Identify the blood parasite species.
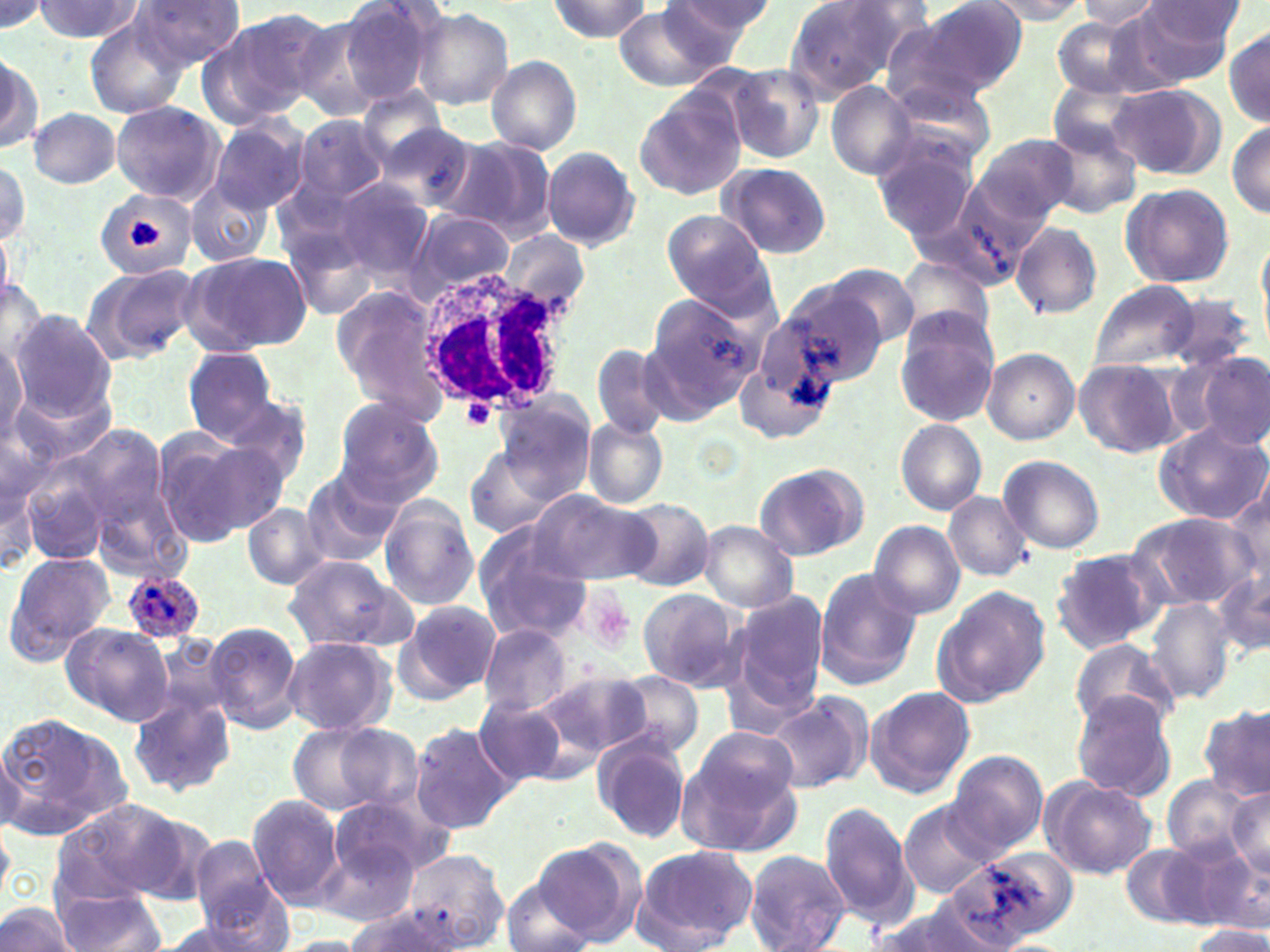
Plasmodium ovale.

Approximate bounding boxes as named x1/y1/x2/y2 corners in pixels. White blood cell locations: (x1=414, y1=260, x2=575, y2=418). Plasmodium ovale-infected red blood cell locations: (x1=122, y1=568, x2=205, y2=644). Platelet locations: (x1=130, y1=219, x2=160, y2=250), (x1=461, y1=399, x2=498, y2=433), (x1=582, y1=593, x2=634, y2=654). Uninfected red blood cell locations: (x1=337, y1=0, x2=446, y2=106), (x1=665, y1=0, x2=772, y2=55), (x1=782, y1=0, x2=915, y2=101), (x1=910, y1=0, x2=1028, y2=97), (x1=982, y1=0, x2=1092, y2=24), (x1=1076, y1=0, x2=1164, y2=30), (x1=35, y1=1, x2=142, y2=42), (x1=131, y1=1, x2=245, y2=71), (x1=547, y1=1, x2=652, y2=40), (x1=0, y1=2, x2=45, y2=31), (x1=612, y1=3, x2=737, y2=88), (x1=1131, y1=3, x2=1240, y2=83), (x1=411, y1=8, x2=513, y2=110), (x1=200, y1=11, x2=327, y2=123), (x1=83, y1=17, x2=190, y2=120), (x1=1051, y1=18, x2=1151, y2=98), (x1=880, y1=21, x2=1003, y2=120), (x1=1224, y1=26, x2=1269, y2=128), (x1=1, y1=54, x2=41, y2=154), (x1=486, y1=55, x2=583, y2=154), (x1=727, y1=64, x2=826, y2=164), (x1=886, y1=75, x2=998, y2=170), (x1=1049, y1=78, x2=1150, y2=159), (x1=828, y1=82, x2=916, y2=181), (x1=1106, y1=83, x2=1222, y2=179), (x1=636, y1=90, x2=743, y2=198), (x1=109, y1=100, x2=224, y2=204), (x1=28, y1=107, x2=121, y2=188), (x1=209, y1=117, x2=310, y2=215), (x1=293, y1=117, x2=387, y2=202), (x1=1228, y1=119, x2=1269, y2=219), (x1=374, y1=122, x2=483, y2=217), (x1=1044, y1=125, x2=1142, y2=220), (x1=974, y1=133, x2=1079, y2=227), (x1=872, y1=135, x2=980, y2=241), (x1=441, y1=136, x2=556, y2=241), (x1=543, y1=148, x2=640, y2=250), (x1=0, y1=158, x2=30, y2=246), (x1=717, y1=162, x2=831, y2=259), (x1=954, y1=173, x2=1061, y2=269), (x1=327, y1=176, x2=437, y2=288), (x1=186, y1=179, x2=273, y2=269), (x1=1121, y1=183, x2=1235, y2=289), (x1=95, y1=190, x2=197, y2=279), (x1=409, y1=210, x2=515, y2=297), (x1=661, y1=211, x2=774, y2=314), (x1=1011, y1=222, x2=1102, y2=320), (x1=502, y1=229, x2=587, y2=316), (x1=181, y1=250, x2=311, y2=357), (x1=898, y1=256, x2=994, y2=352), (x1=83, y1=263, x2=198, y2=362), (x1=821, y1=263, x2=919, y2=350), (x1=0, y1=274, x2=48, y2=373), (x1=1088, y1=280, x2=1200, y2=372), (x1=782, y1=284, x2=886, y2=385), (x1=331, y1=287, x2=452, y2=419), (x1=646, y1=290, x2=766, y2=408), (x1=1161, y1=291, x2=1257, y2=374), (x1=9, y1=310, x2=117, y2=419), (x1=895, y1=311, x2=1000, y2=427), (x1=0, y1=339, x2=29, y2=447), (x1=592, y1=344, x2=671, y2=439), (x1=735, y1=346, x2=835, y2=448), (x1=182, y1=347, x2=281, y2=444), (x1=982, y1=347, x2=1079, y2=444), (x1=1196, y1=355, x2=1269, y2=451), (x1=1074, y1=358, x2=1181, y2=456), (x1=208, y1=389, x2=315, y2=487), (x1=492, y1=389, x2=599, y2=501), (x1=331, y1=397, x2=444, y2=506), (x1=581, y1=417, x2=669, y2=510), (x1=1154, y1=419, x2=1270, y2=525), (x1=896, y1=420, x2=986, y2=513), (x1=152, y1=426, x2=280, y2=545), (x1=77, y1=427, x2=164, y2=526), (x1=465, y1=447, x2=560, y2=541), (x1=0, y1=452, x2=38, y2=578), (x1=998, y1=455, x2=1105, y2=555), (x1=754, y1=462, x2=867, y2=562), (x1=298, y1=467, x2=405, y2=568), (x1=26, y1=473, x2=105, y2=562), (x1=1224, y1=485, x2=1270, y2=593), (x1=530, y1=490, x2=659, y2=586), (x1=943, y1=492, x2=1033, y2=582), (x1=376, y1=497, x2=480, y2=611), (x1=96, y1=499, x2=191, y2=579), (x1=618, y1=499, x2=714, y2=592), (x1=243, y1=503, x2=328, y2=590), (x1=1130, y1=512, x2=1251, y2=609), (x1=699, y1=521, x2=799, y2=611), (x1=869, y1=522, x2=966, y2=619), (x1=472, y1=527, x2=593, y2=641), (x1=1049, y1=550, x2=1163, y2=655), (x1=2, y1=552, x2=116, y2=668), (x1=281, y1=554, x2=411, y2=651), (x1=1213, y1=564, x2=1270, y2=662), (x1=813, y1=568, x2=922, y2=688), (x1=933, y1=586, x2=1051, y2=708), (x1=637, y1=588, x2=745, y2=691), (x1=727, y1=590, x2=829, y2=716), (x1=1146, y1=598, x2=1235, y2=705), (x1=395, y1=600, x2=501, y2=704), (x1=205, y1=621, x2=304, y2=734), (x1=61, y1=623, x2=174, y2=725), (x1=478, y1=625, x2=575, y2=716), (x1=147, y1=633, x2=234, y2=727), (x1=281, y1=636, x2=396, y2=737), (x1=1069, y1=638, x2=1178, y2=733), (x1=538, y1=669, x2=650, y2=766), (x1=613, y1=671, x2=704, y2=761), (x1=865, y1=685, x2=976, y2=798), (x1=762, y1=691, x2=873, y2=794), (x1=1070, y1=692, x2=1177, y2=800), (x1=128, y1=695, x2=234, y2=797), (x1=473, y1=695, x2=571, y2=789), (x1=1200, y1=704, x2=1269, y2=801), (x1=0, y1=710, x2=129, y2=839), (x1=286, y1=721, x2=405, y2=816), (x1=411, y1=722, x2=518, y2=834), (x1=593, y1=731, x2=693, y2=843), (x1=0, y1=742, x2=25, y2=834), (x1=675, y1=742, x2=802, y2=857), (x1=947, y1=752, x2=1048, y2=855), (x1=1162, y1=775, x2=1257, y2=863), (x1=1041, y1=776, x2=1157, y2=880), (x1=1225, y1=785, x2=1270, y2=883), (x1=330, y1=793, x2=449, y2=882), (x1=248, y1=794, x2=346, y2=907), (x1=55, y1=799, x2=185, y2=905), (x1=898, y1=802, x2=993, y2=897), (x1=819, y1=803, x2=917, y2=928), (x1=0, y1=821, x2=13, y2=906), (x1=186, y1=835, x2=279, y2=928), (x1=1132, y1=836, x2=1256, y2=932), (x1=531, y1=840, x2=645, y2=945), (x1=317, y1=842, x2=417, y2=926), (x1=630, y1=845, x2=759, y2=952), (x1=400, y1=848, x2=507, y2=952), (x1=742, y1=850, x2=852, y2=952), (x1=948, y1=852, x2=1077, y2=944), (x1=195, y1=874, x2=294, y2=952), (x1=503, y1=878, x2=592, y2=952), (x1=55, y1=890, x2=165, y2=952), (x1=0, y1=902, x2=77, y2=952), (x1=864, y1=904, x2=1006, y2=952), (x1=344, y1=906, x2=459, y2=952), (x1=152, y1=917, x2=269, y2=952), (x1=1188, y1=925, x2=1270, y2=951), (x1=280, y1=936, x2=375, y2=951). One field of a larger specimen. Light microscopy. May-Grünwald-Giemsa-stained preparation. Captured at 1000x magnification. Thin blood film. Image is 1270×952 pixels.